Identify the parasite.
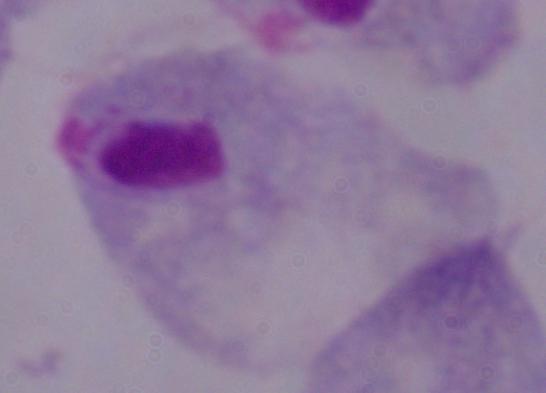
This is a trichomonad.

Summary:
  - Magnification: 1000x
  - Modality: photomicrograph